Comment on the morphology of the erythrocytes.
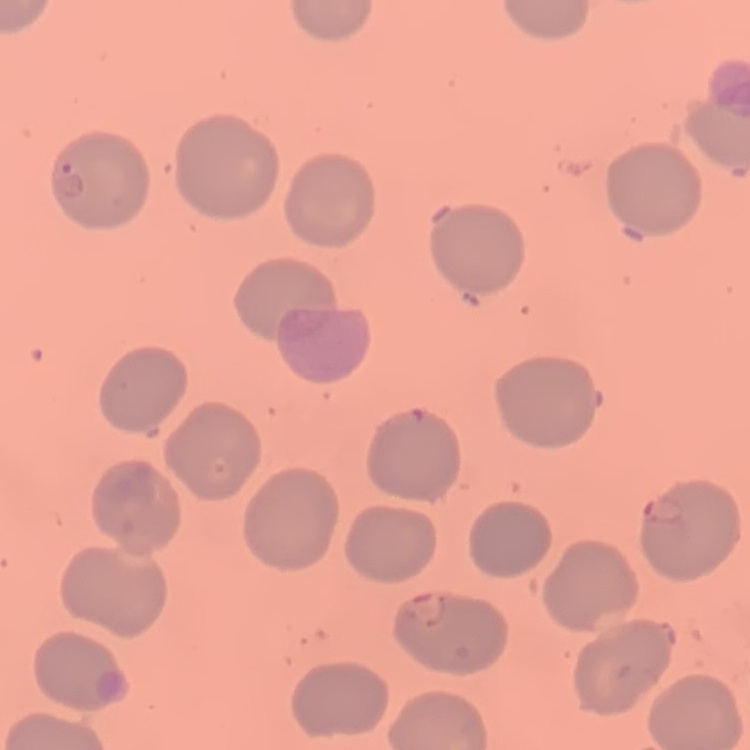

No rouleaux formation.

stain = Field's or Giemsa
preparation = thin peripheral smear
image type = one tile cut from a larger photomicrograph